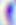
400x magnification. Photomicrograph. Toxoplasma gondii is seen.